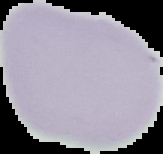

Image is 163×154 pixels. From a thin blood film. Malaria status: uninfected. Segmented cell region on a black background.